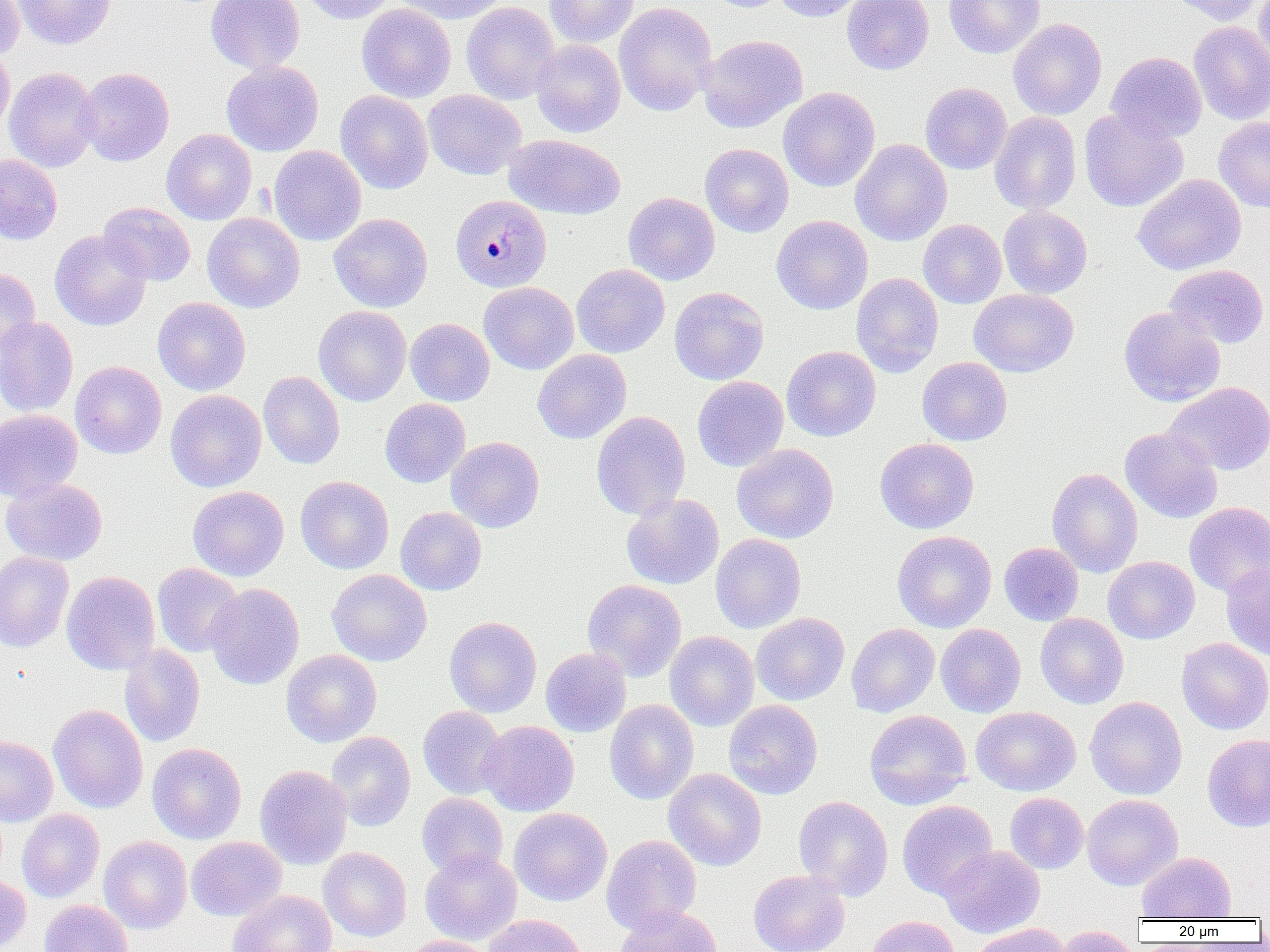
slide_level_diagnosis: Plasmodium malariae
modality: light microscopy
preparation: thin blood smear
image_size: 1270×952 pixels
field_of_view: one of a larger specimen
plasmodium_malariae_infected_red_blood_cell_locations: 'approximate bounding boxes as (x1,y1)-(x2,y2) corner pairs in pixels: (450,194)-(552,292)'
uninfected_red_blood_cell_locations: 'approximate bounding boxes as (x1,y1)-(x2,y2) corner pairs in pixels: (0,0)-(24,60), (13,0)-(115,49), (206,0)-(305,74), (302,0)-(397,24), (391,0)-(509,24), (545,0)-(639,47), (707,0)-(790,12), (772,0)-(867,22), (841,0)-(933,75), (944,0)-(1045,59), (1166,0)-(1263,26), (1254,0)-(1270,71), (461,2)-(560,105), (614,2)-(717,116), (356,3)-(456,103), (1008,18)-(1107,120), (1188,21)-(1270,125), (697,34)-(808,133), (531,40)-(626,137), (0,44)-(14,136), (1106,51)-(1206,143), (221,61)-(324,156), (4,67)-(101,172), (76,67)-(174,166), (920,82)-(1012,174), (778,87)-(879,192), (335,90)-(433,193), (423,90)-(526,180), (1079,109)-(1189,212), (989,111)-(1081,215), (1213,117)-(1270,213), (161,129)-(257,225), (504,134)-(626,219), (850,138)-(952,246), (700,143)-(793,237), (268,145)-(366,246), (0,153)-(62,245), (1133,173)-(1246,275), (623,192)-(720,285), (98,202)-(195,286), (998,206)-(1092,298), (202,213)-(305,312), (328,213)-(433,312), (771,215)-(873,315), (918,219)-(1007,309), (49,230)-(152,331), (571,264)-(670,358), (1164,264)-(1269,348), (0,266)-(41,360), (851,273)-(944,377), (479,282)-(579,374), (669,287)-(769,385), (969,288)-(1078,377), (153,297)-(251,396), (313,305)-(412,406), (1119,306)-(1226,407), (0,317)-(78,417), (405,318)-(495,406), (782,345)-(881,441), (532,349)-(632,444), (917,357)-(1012,446), (70,361)-(167,459), (258,371)-(345,469), (692,376)-(788,472), (1165,382)-(1270,475), (165,390)-(267,492), (380,398)-(470,487), (0,408)-(82,501), (591,411)-(691,520), (1120,427)-(1222,523), (446,437)-(544,533), (875,438)-(979,533), (732,444)-(839,543), (1046,468)-(1143,577), (295,475)-(394,574), (1,477)-(107,566), (188,485)-(289,581), (621,493)-(724,590), (1184,501)-(1270,597), (395,507)-(486,595), (892,530)-(996,632), (710,533)-(806,633), (999,542)-(1083,625), (0,552)-(73,652), (1103,556)-(1199,644), (1221,561)-(1270,661), (152,563)-(244,657), (327,569)-(432,666), (61,570)-(160,675), (582,579)-(686,681), (205,582)-(304,690), (751,613)-(850,705), (1035,613)-(1128,709), (444,616)-(542,717), (846,623)-(939,717), (935,623)-(1026,717), (665,631)-(759,731), (1177,637)-(1270,734), (119,644)-(205,747), (540,648)-(631,737), (281,649)-(381,747), (1085,696)-(1188,800), (604,700)-(699,804), (724,700)-(823,799), (48,704)-(148,813), (417,706)-(508,799), (971,706)-(1081,796), (864,709)-(972,810), (480,720)-(579,816), (326,731)-(415,831), (1202,733)-(1270,832), (0,735)-(58,826), (147,742)-(247,844), (255,764)-(352,869), (663,768)-(766,871), (1005,792)-(1089,874), (417,793)-(508,878), (1082,794)-(1183,890), (793,795)-(893,900), (897,800)-(997,900), (509,808)-(612,906), (17,809)-(104,902), (601,834)-(702,934), (99,836)-(192,934), (186,836)-(287,921), (939,845)-(1045,938), (318,847)-(411,942), (419,849)-(521,945), (1137,852)-(1236,920), (748,869)-(850,952), (0,872)-(31,951), (227,890)-(337,952), (39,899)-(133,952), (614,905)-(723,952), (484,914)-(586,952), (863,915)-(961,952), (969,923)-(1071,952), (1053,925)-(1140,952), (399,935)-(494,952)'
magnification: 1000x